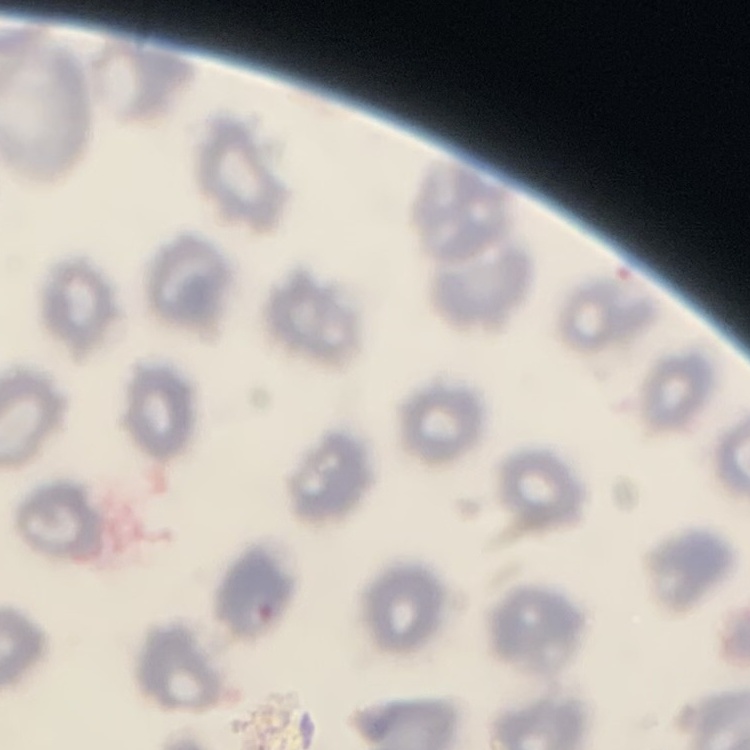

Summary:
  - Erythrocyte morphology: no rouleaux formation
  - Image type: square crop of a larger photomicrograph
  - Stain: Field's or Giemsa
  - Preparation: thin peripheral smear